Report the malaria status of this cell.
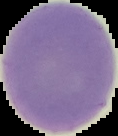
Uninfected.

{
  "image_size": "118×136 pixels",
  "image_type": "cell region segmented out of the field of view; surrounding area masked to black",
  "preparation": "thin blood smear"
}